Locate platelets.
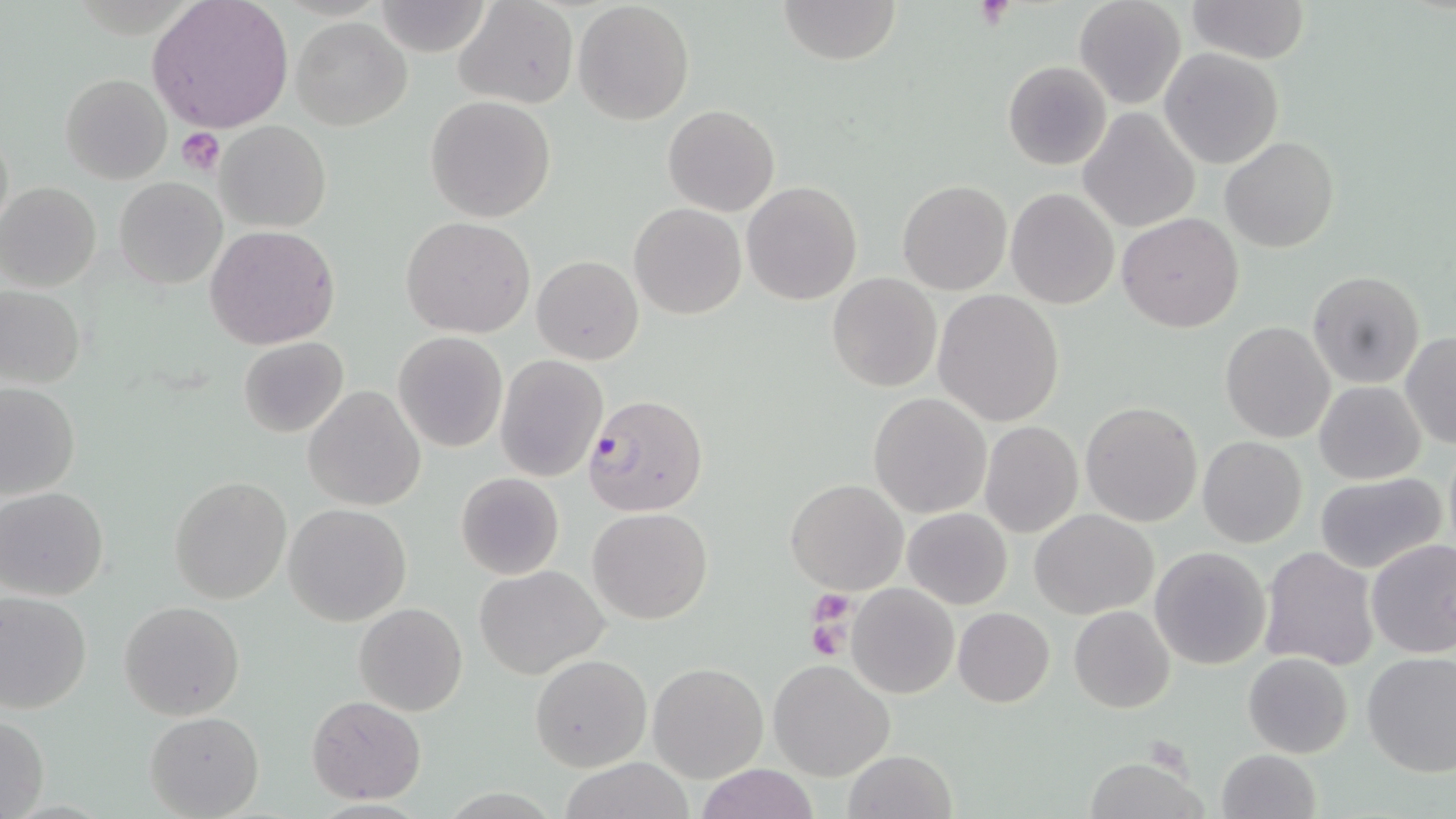

Approximate bounding boxes as (x1,y1)-(x2,y2) corner pairs in pixels.
Platelets: (176,128)-(226,176), (808,589)-(856,635), (806,618)-(849,661).

Summary:
  - Uninfected red blood cell locations: (454,0)-(579,111), (778,0)-(903,65), (1074,0)-(1187,110), (1185,0)-(1311,65), (146,1)-(295,133), (574,3)-(693,125), (291,18)-(412,130), (1160,47)-(1286,169), (1002,59)-(1112,169), (59,72)-(172,184), (425,95)-(556,221), (663,104)-(780,216), (1078,109)-(1199,231), (216,120)-(331,232), (1221,137)-(1339,255), (114,177)-(225,288), (898,180)-(1011,293), (741,181)-(863,304), (0,182)-(102,292), (1005,188)-(1120,311), (629,202)-(745,319), (1118,212)-(1243,332), (401,217)-(535,337), (205,225)-(341,351), (532,255)-(643,366), (1307,271)-(1427,389), (827,273)-(942,392), (0,286)-(85,389), (933,291)-(1064,425), (1221,320)-(1335,442), (392,332)-(508,454), (1401,332)-(1455,448), (238,338)-(349,437), (495,355)-(608,482), (0,382)-(81,501), (1315,382)-(1426,484), (303,385)-(427,511), (868,392)-(993,518), (1079,400)-(1203,527), (979,420)-(1084,538), (1197,437)-(1308,547), (456,471)-(565,580), (1314,472)-(1448,574), (169,476)-(292,604), (785,478)-(909,595), (1,487)-(113,601), (284,504)-(412,626), (903,507)-(1012,609), (587,508)-(713,625), (1032,508)-(1158,618), (1366,539)-(1456,659), (1259,546)-(1379,670), (1149,547)-(1271,668), (473,565)-(609,679), (847,582)-(958,698), (0,591)-(93,714), (119,600)-(245,720), (354,602)-(467,716), (954,607)-(1055,707), (1068,607)-(1174,713), (1361,651)-(1455,776), (530,653)-(652,772), (1243,653)-(1353,757), (768,659)-(895,781), (649,662)-(767,782), (306,694)-(427,805), (145,711)-(264,818), (0,712)-(48,819), (843,750)-(956,819), (1216,750)-(1321,819), (1085,755)-(1208,819), (555,759)-(699,818), (695,765)-(819,819)
  - Plasmodium falciparum-infected red blood cell locations: (583,393)-(708,515)
  - Slide-level diagnosis: Plasmodium falciparum
  - Magnification: 1000x
  - Field of view: one of a larger specimen
  - Stain: May-Grünwald-Giemsa
  - Preparation: thin blood smear
  - Modality: optical microscopy
  - Image size: 1456×819 pixels